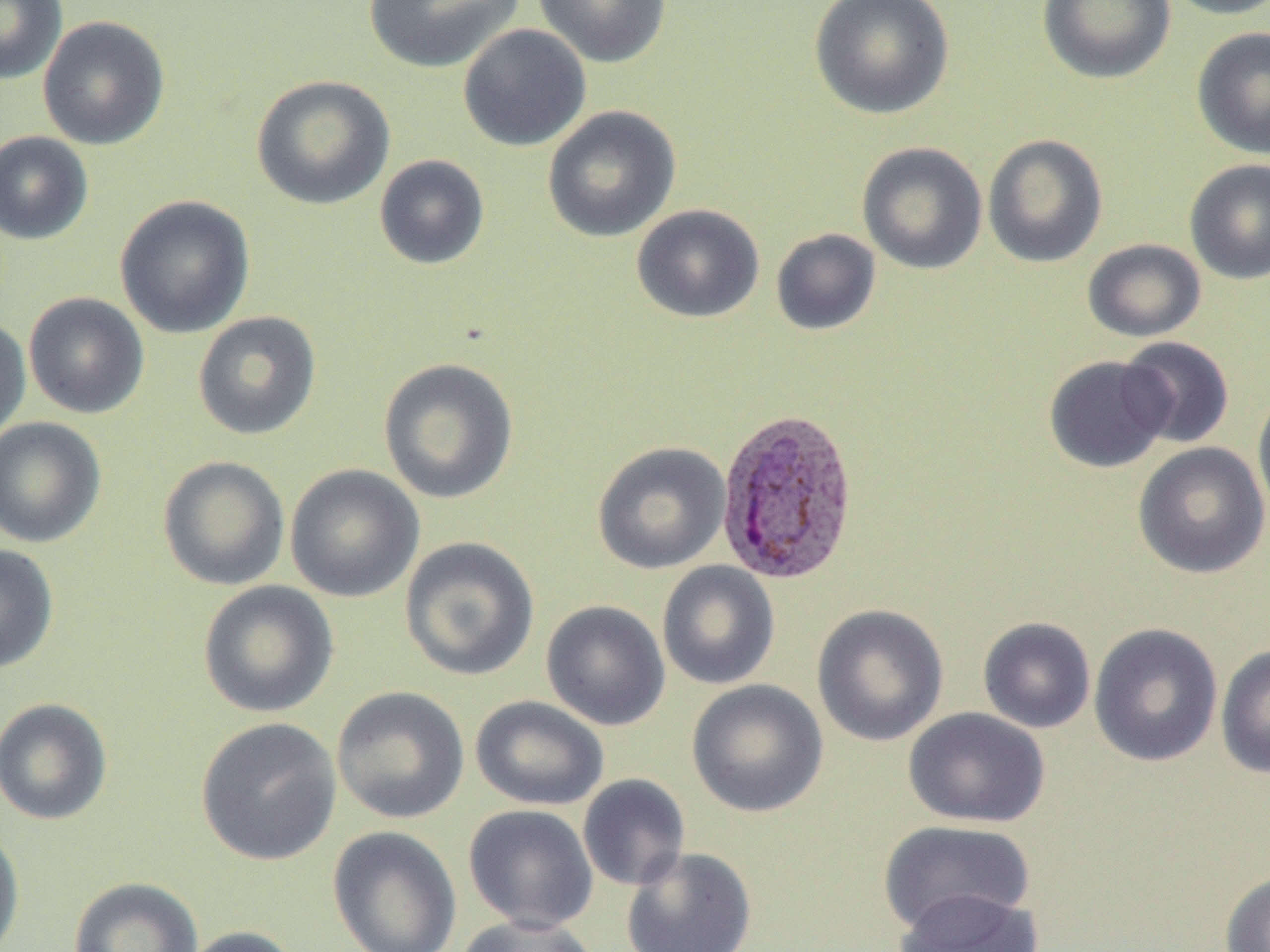

slide-level diagnosis = Plasmodium vivax
uninfected red blood cell locations = approximate bounding boxes as [x1, y1, x2, y2] in pixels: [0, 0, 67, 85], [363, 0, 526, 73], [534, 0, 672, 68], [809, 0, 955, 120], [1037, 0, 1176, 84], [1162, 0, 1270, 20], [37, 15, 170, 151], [457, 24, 591, 152], [1191, 26, 1270, 159], [251, 74, 395, 210], [541, 105, 681, 243], [0, 130, 94, 245], [982, 134, 1108, 268], [856, 141, 988, 275], [374, 154, 490, 270], [1184, 159, 1270, 285], [114, 195, 255, 339], [631, 204, 765, 323], [771, 228, 881, 336], [1082, 238, 1207, 342], [23, 292, 150, 419], [192, 311, 322, 440], [0, 316, 31, 445], [1117, 336, 1235, 449], [1043, 355, 1173, 473], [377, 357, 520, 505], [1252, 385, 1270, 523], [0, 417, 107, 548], [591, 441, 731, 574], [1132, 442, 1269, 579], [157, 455, 290, 591], [284, 464, 424, 603], [399, 536, 540, 681], [0, 543, 59, 674], [656, 561, 780, 690], [197, 580, 339, 718], [541, 600, 671, 731], [811, 604, 949, 747], [977, 617, 1096, 734], [1088, 622, 1223, 767], [1215, 644, 1270, 778], [686, 679, 829, 818], [331, 686, 470, 824], [470, 695, 610, 811], [0, 697, 113, 825], [903, 707, 1050, 828], [195, 716, 342, 866], [577, 774, 690, 891], [463, 804, 599, 932], [0, 820, 25, 952], [876, 820, 1036, 936], [327, 826, 463, 952], [621, 846, 757, 952], [1220, 870, 1270, 952], [68, 876, 204, 952], [895, 887, 1042, 952], [453, 914, 600, 951], [177, 925, 303, 952]
magnification = 1000x
preparation = thin blood smear
Plasmodium vivax-infected red blood cell locations = approximate bounding boxes as [x1, y1, x2, y2] in pixels: [716, 407, 861, 586]
image size = 1270×952 pixels
field of view = single
modality = optical microscopy